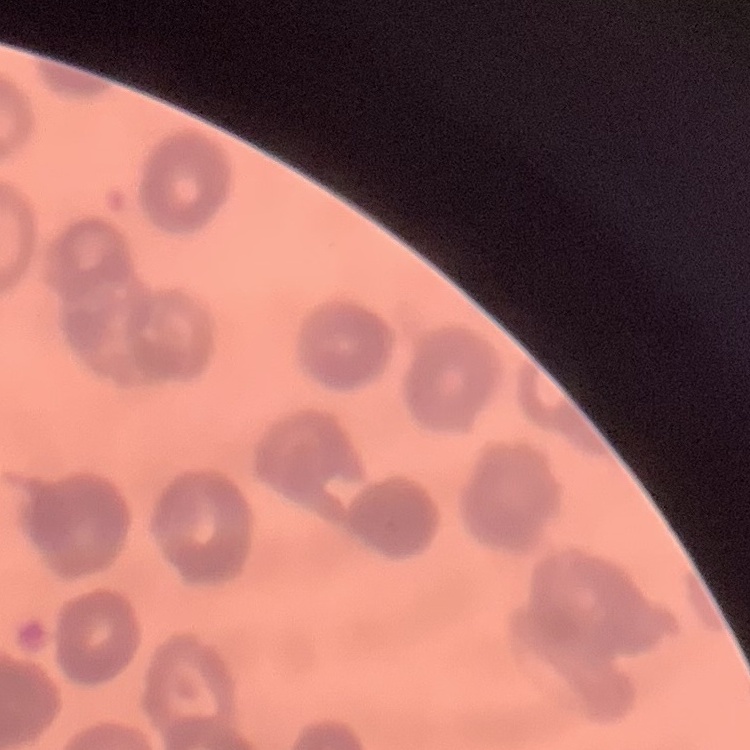
The erythrocytes exhibit rouleaux formation. Thin blood smear. Square crop of a larger photomicrograph. Stained with either Field's or Giemsa.